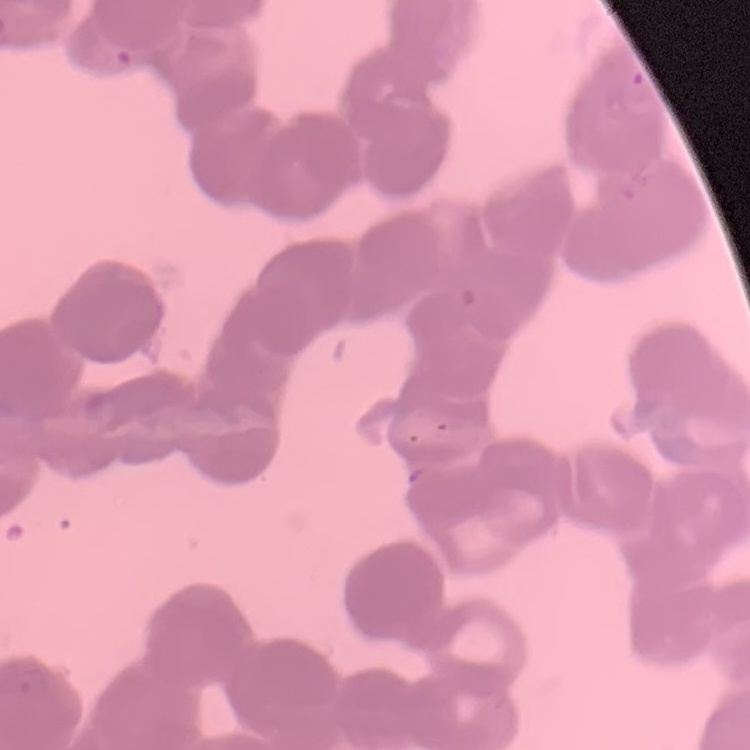 The erythrocytes exhibit rouleaux formation. Thin blood smear. One tile cut from a larger photomicrograph. Field's or Giemsa stain.